Identify the parasite.
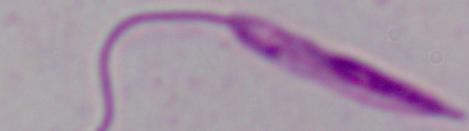
This is Leishmania.

Photomicrograph. 1000x magnification.